Comment on the morphology of the erythrocytes.
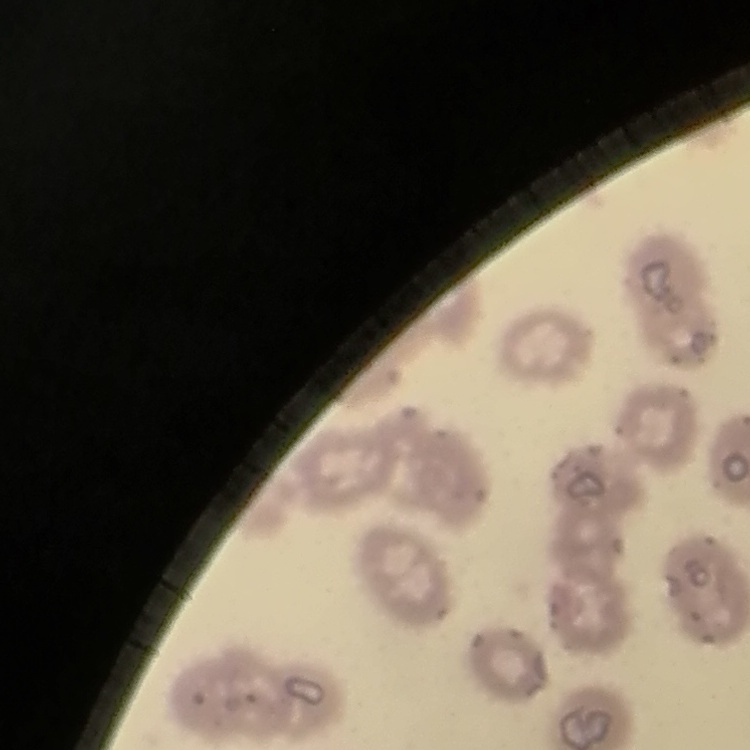

They show no rouleaux formation.

image type = square crop of a larger photomicrograph
preparation = thin blood film
stain = Field's or Giemsa